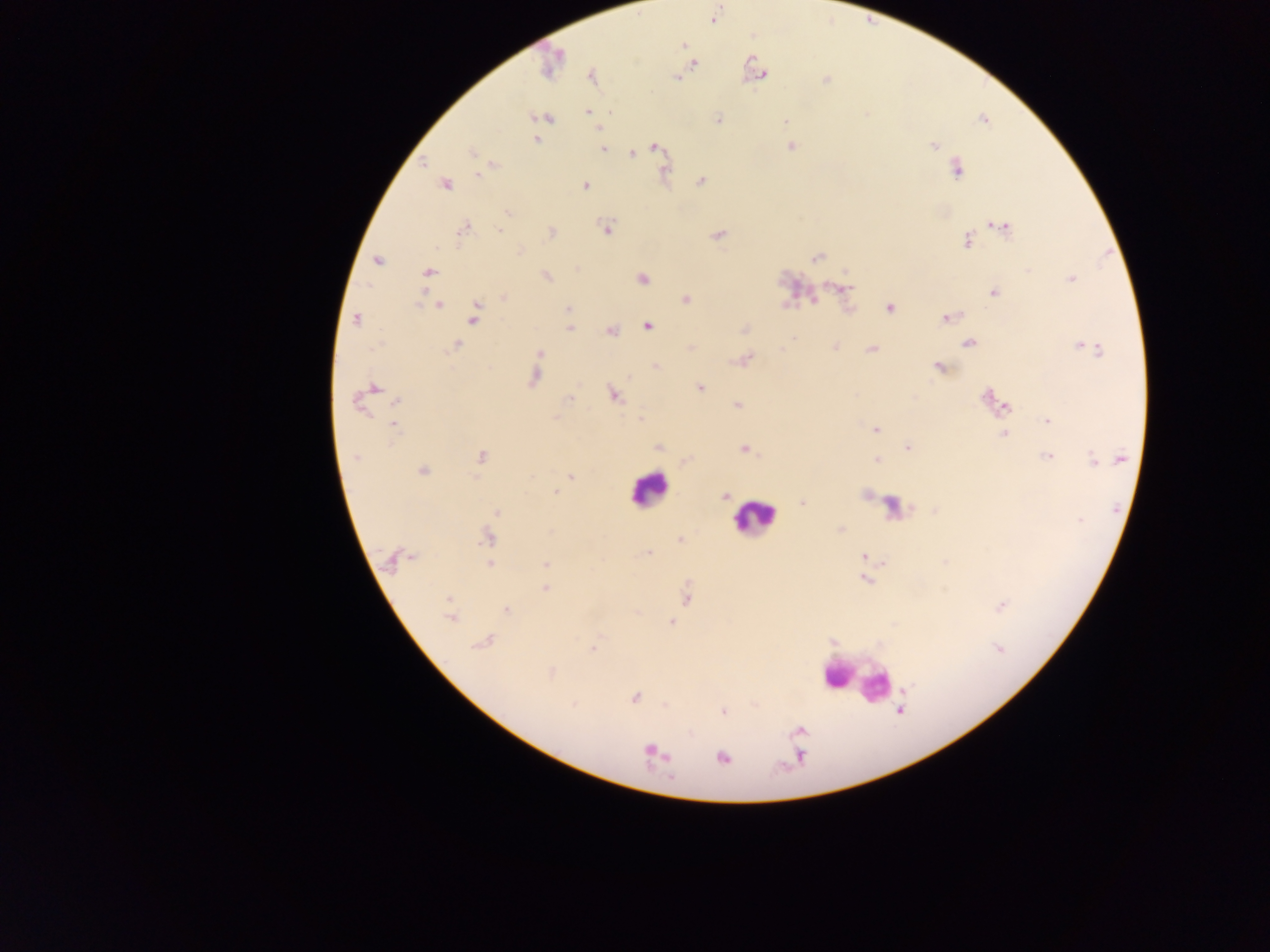
Approximate centers as (x, y) in pixels. Plasmodium parasite locations: (712, 20), (685, 46), (693, 64), (759, 73), (764, 74), (676, 75), (826, 80), (588, 111), (866, 114), (718, 119), (784, 120), (536, 138), (655, 146), (933, 146), (605, 148), (790, 148), (473, 153), (632, 154), (425, 160), (956, 167), (665, 170), (702, 180), (447, 184), (583, 184), (507, 213), (1006, 227), (464, 229), (606, 229), (501, 230), (551, 231), (718, 234), (965, 241), (520, 250), (816, 257), (378, 260), (577, 266), (1027, 269), (430, 272), (546, 275), (1071, 278), (642, 279), (832, 284), (847, 287), (993, 293), (504, 297), (686, 298), (813, 299), (787, 302), (479, 304), (439, 306), (567, 307), (890, 308), (474, 314), (945, 317), (355, 320), (473, 322), (648, 326), (569, 328), (742, 328), (611, 330), (794, 339), (967, 343), (455, 345), (835, 345), (1087, 345), (690, 346), (781, 348), (871, 349), (539, 353), (739, 360), (747, 360), (656, 364), (938, 368), (534, 379), (378, 386), (701, 387), (613, 394), (570, 399), (396, 401), (986, 401), (358, 402), (736, 405), (640, 418), (1046, 421), (394, 426), (876, 429), (1004, 434), (658, 446), (908, 447), (742, 449), (355, 455), (481, 456), (1047, 456), (1091, 457), (877, 459), (1118, 459), (686, 460), (421, 471), (531, 475), (569, 476), (474, 477), (556, 492), (865, 494), (724, 497), (802, 502), (496, 512), (840, 529), (485, 537), (679, 538), (646, 552), (412, 557), (863, 557), (397, 560), (387, 561), (944, 561), (490, 564), (545, 564), (865, 579), (545, 589), (943, 589), (448, 599), (686, 599), (1001, 607), (506, 608), (451, 619), (671, 622), (485, 640), (477, 643), (592, 647), (998, 649), (552, 673), (906, 688), (635, 698), (755, 704), (665, 705), (899, 710), (723, 711), (648, 751), (666, 756), (722, 758). Leukocyte locations: (649, 494), (757, 520), (840, 668), (873, 679). Single field of view. Image is 1270×952 pixels. Thick blood smear. Photographed through a microscope with a mobile-phone camera. Sample from Ghana.